Assess this cell for malaria.
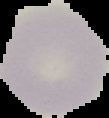
Uninfected.

Image is 109×118 pixels. Cell region segmented out of the field of view; the surrounding area is masked to black. From a thin blood film.